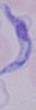

{
  "magnification": "1000x",
  "modality": "photomicrograph",
  "identification": "trypanosome"
}